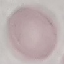

{
  "result": "no malaria parasites seen",
  "capture": "smartphone camera at the microscope eyepiece",
  "image_type": "automatically extracted cell patch, resized to 64 × 64 pixels",
  "preparation": "thin blood film",
  "stain": "Giemsa"
}